Assess the morphology of the erythrocytes.
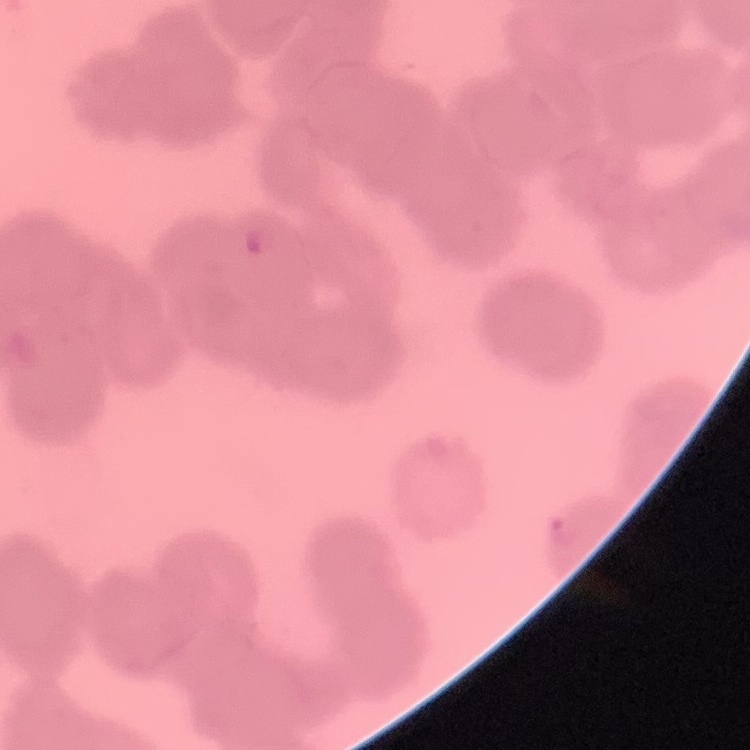
Rouleaux formation.

Summary:
  - Preparation: thin blood film
  - Image type: one tile cut from a larger photomicrograph
  - Stain: Field's or Giemsa